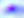
Toxoplasma gondii is shown. 400x magnification. Photomicrograph.